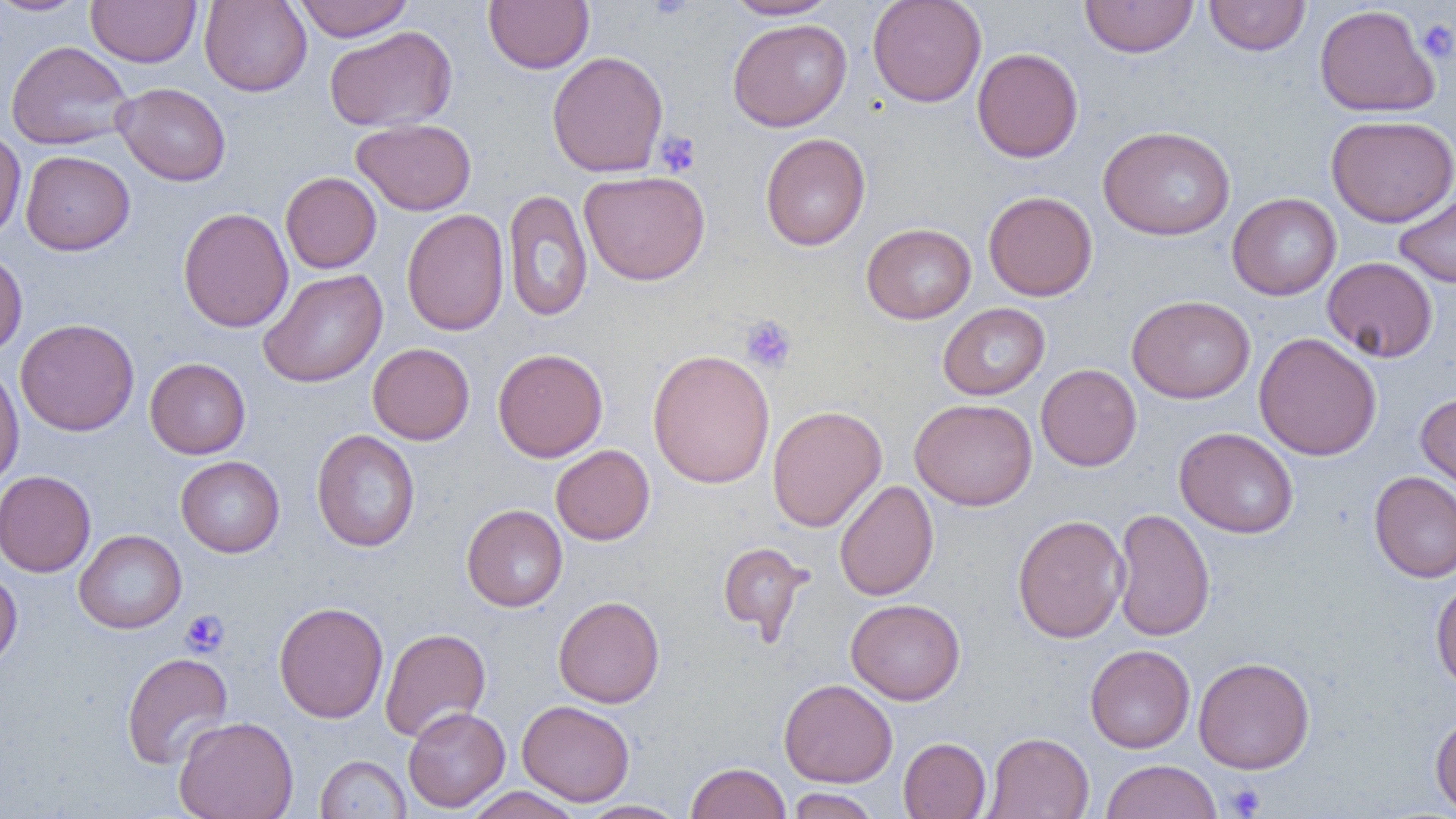
Approximate bounding boxes as (x1,y1)-(x2,y2) corner pairs in pixels. Platelet locations: (1416,19)-(1456,63), (655,131)-(702,178), (740,315)-(797,373), (181,610)-(229,657), (1223,782)-(1266,817). Uninfected red blood cell locations: (0,0)-(91,16), (86,0)-(202,67), (293,0)-(414,41), (484,0)-(594,73), (725,0)-(839,20), (867,0)-(987,107), (1080,0)-(1198,58), (1204,0)-(1310,56), (199,1)-(312,96), (1314,4)-(1439,117), (727,18)-(852,131), (324,26)-(457,132), (6,40)-(133,150), (972,47)-(1083,162), (547,50)-(669,177), (113,82)-(231,186), (1326,114)-(1456,227), (351,118)-(476,216), (1099,125)-(1236,241), (0,127)-(26,243), (760,133)-(870,250), (21,150)-(135,255), (579,170)-(710,285), (280,171)-(381,273), (1394,188)-(1456,288), (503,189)-(593,321), (983,190)-(1098,301), (1227,193)-(1341,300), (177,207)-(293,332), (401,209)-(509,336), (861,223)-(976,324), (0,247)-(28,358), (1322,257)-(1438,362), (258,269)-(388,388), (1127,294)-(1255,404), (938,303)-(1050,400), (15,318)-(140,436), (1254,332)-(1382,461), (367,343)-(475,445), (492,348)-(608,462), (648,348)-(776,489), (145,358)-(251,459), (0,362)-(24,490), (1035,364)-(1142,471), (1416,392)-(1456,497), (910,398)-(1037,511), (767,405)-(887,532), (1174,427)-(1299,539), (311,429)-(420,552), (551,444)-(655,545), (175,456)-(285,557), (0,470)-(96,577), (1369,471)-(1456,583), (834,480)-(938,601), (461,504)-(567,612), (1112,508)-(1215,642), (1012,514)-(1129,643), (74,529)-(187,633), (717,542)-(811,641), (0,569)-(22,671), (1431,578)-(1456,692), (553,595)-(665,708), (846,598)-(965,705), (273,601)-(388,723), (379,626)-(491,743), (1085,644)-(1195,753), (121,652)-(233,769), (1193,657)-(1314,773), (779,678)-(897,787), (517,700)-(635,806), (402,706)-(510,812), (1430,713)-(1456,815), (174,715)-(299,819), (984,731)-(1094,819), (899,737)-(991,818), (315,755)-(410,818), (1101,759)-(1222,819), (686,761)-(791,819), (464,786)-(584,819), (787,788)-(881,818), (576,800)-(687,818). Slide-level diagnosis: no evidence of blood parasites. Image is 1456×819 pixels. Optical microscopy. Thin blood film. One field of a larger specimen. 1000x magnification.